Name the parasite shown.
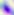

This is Toxoplasma gondii.

Photomicrograph. Captured at 400x magnification.